Point out each leukocyte.
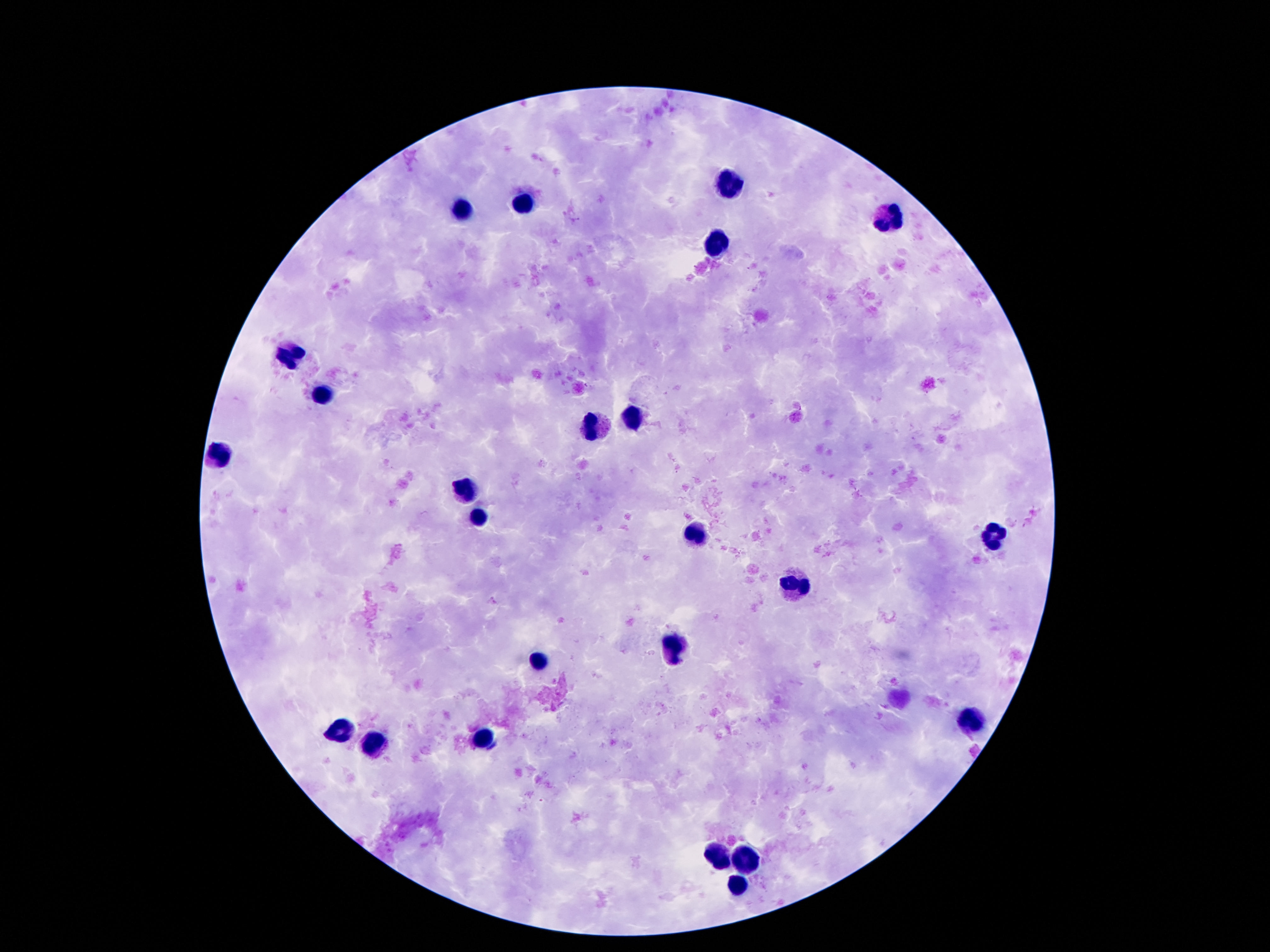

Approximate object centers, in pixels from the top-left corner.
Leukocytes: (x=730, y=179), (x=528, y=205), (x=462, y=208), (x=888, y=220), (x=716, y=244), (x=289, y=354), (x=323, y=394), (x=630, y=420), (x=594, y=430), (x=219, y=456), (x=468, y=488), (x=476, y=516), (x=696, y=534), (x=992, y=538), (x=794, y=585), (x=674, y=650), (x=540, y=665), (x=970, y=722), (x=339, y=731), (x=482, y=736), (x=376, y=748), (x=720, y=858), (x=746, y=861), (x=738, y=885).

stain = Giemsa
field of view = single
patient malaria status = uninfected
magnification = 100x
image size = 1270×952 pixels
capture = smartphone camera through the microscope eyepiece
preparation = thick blood film